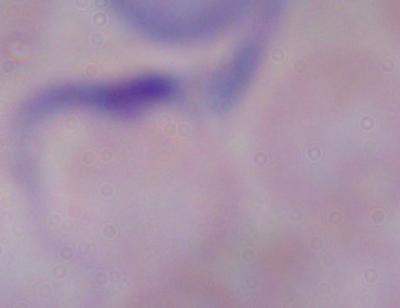
A trypanosome is seen. Photomicrograph. Captured at 1000x magnification.